Identify the parasite.
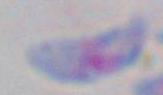

This is Toxoplasma gondii.

Summary:
  - Magnification: 1000x
  - Modality: micrograph